Identify the parasite.
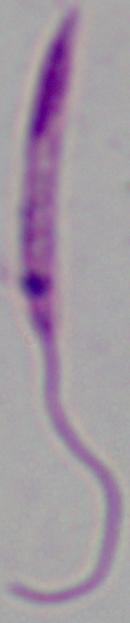
Leishmania.

Captured at 1000x magnification. Photomicrograph.